Locate every Plasmodium parasite.
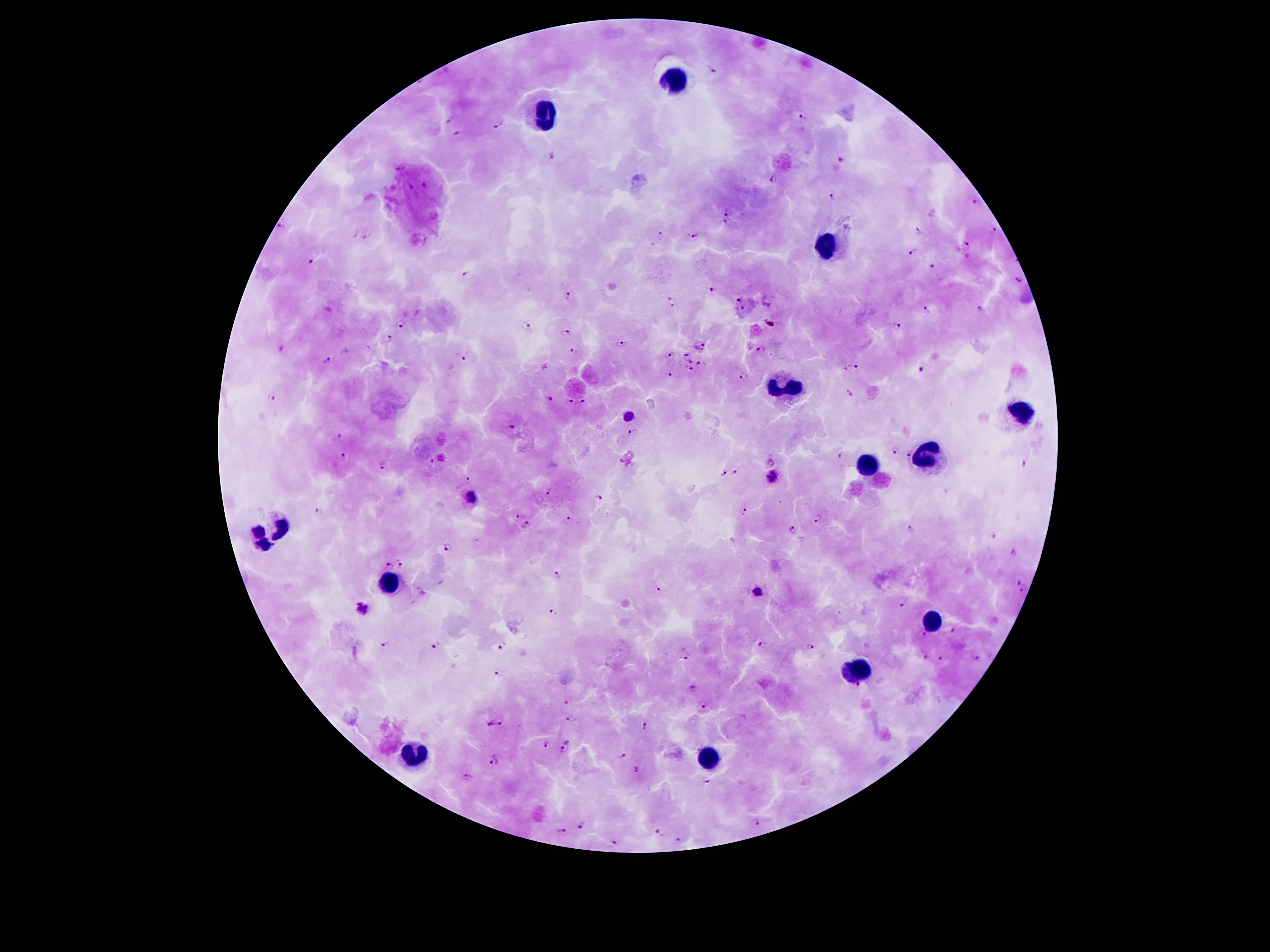
Approximate centers as {x, y} in pixels.
Plasmodium parasites: {713, 69}, {450, 118}, {804, 118}, {499, 122}, {459, 132}, {552, 156}, {840, 160}, {398, 168}, {772, 179}, {424, 185}, {411, 186}, {830, 197}, {976, 203}, {727, 210}, {725, 224}, {279, 225}, {992, 229}, {917, 231}, {367, 233}, {354, 235}, {662, 236}, {694, 236}, {966, 246}, {913, 252}, {311, 259}, {933, 267}, {466, 275}, {1020, 281}, {713, 289}, {568, 294}, {739, 298}, {671, 302}, {743, 308}, {928, 310}, {980, 310}, {401, 325}, {896, 325}, {525, 326}, {564, 334}, {386, 338}, {622, 343}, {700, 346}, {281, 347}, {575, 350}, {762, 350}, {685, 354}, {672, 356}, {461, 357}, {327, 360}, {691, 360}, {702, 365}, {855, 366}, {688, 367}, {921, 369}, {669, 375}, {745, 377}, {850, 393}, {272, 397}, {548, 397}, {585, 400}, {570, 403}, {629, 415}, {511, 425}, {634, 431}, {340, 435}, {895, 450}, {907, 452}, {841, 454}, {343, 456}, {431, 462}, {383, 467}, {736, 472}, {723, 475}, {773, 476}, {468, 480}, {548, 491}, {473, 496}, {597, 498}, {744, 509}, {319, 510}, {818, 517}, {521, 518}, {568, 518}, {529, 525}, {255, 529}, {911, 529}, {792, 531}, {991, 536}, {448, 546}, {265, 550}, {1015, 552}, {388, 564}, {401, 564}, {558, 574}, {1019, 581}, {660, 587}, {1023, 589}, {757, 592}, {902, 604}, {363, 609}, {551, 612}, {954, 630}, {925, 636}, {385, 645}, {763, 645}, {437, 646}, {502, 646}, {810, 646}, {685, 655}, {924, 655}, {942, 659}, {979, 659}, {498, 672}, {693, 685}, {568, 701}, {704, 705}, {572, 719}, {501, 723}, {491, 724}, {645, 724}, {545, 745}, {566, 747}, {623, 752}, {496, 760}, {636, 771}, {468, 776}, {708, 781}, {758, 823}, {581, 825}, {563, 833}, {659, 834}, {681, 840}, {615, 843}.

Summary:
  - Leukocyte locations: {677, 77}, {547, 117}, {826, 245}, {786, 384}, {1022, 411}, {929, 455}, {866, 468}, {280, 527}, {389, 585}, {929, 619}, {857, 670}, {412, 757}, {710, 761}
  - Stain: Giemsa
  - Field of view: single
  - Magnification: 100x
  - Preparation: thick blood smear
  - Image size: 1270×952 pixels
  - Capture: smartphone through the microscope eyepiece
  - Patient malaria status: positive for Plasmodium falciparum